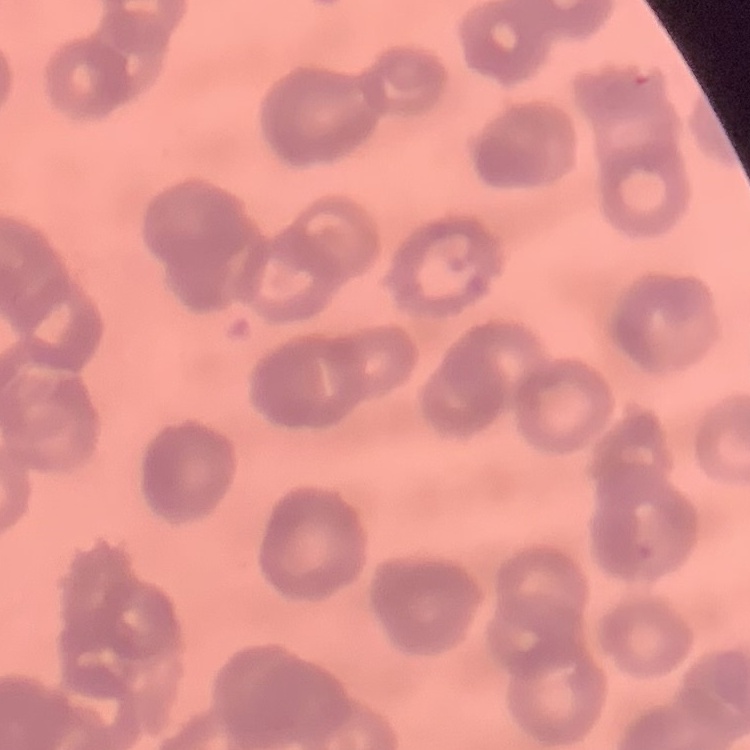

{
  "red_blood_cell_morphology": "rouleaux formation",
  "stain": "Field's or Giemsa",
  "preparation": "thin blood smear",
  "image_type": "one tile cut from a larger photomicrograph"
}